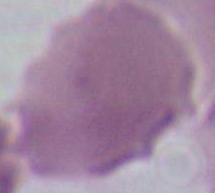
identification = red blood cell
magnification = 1000x
modality = micrograph